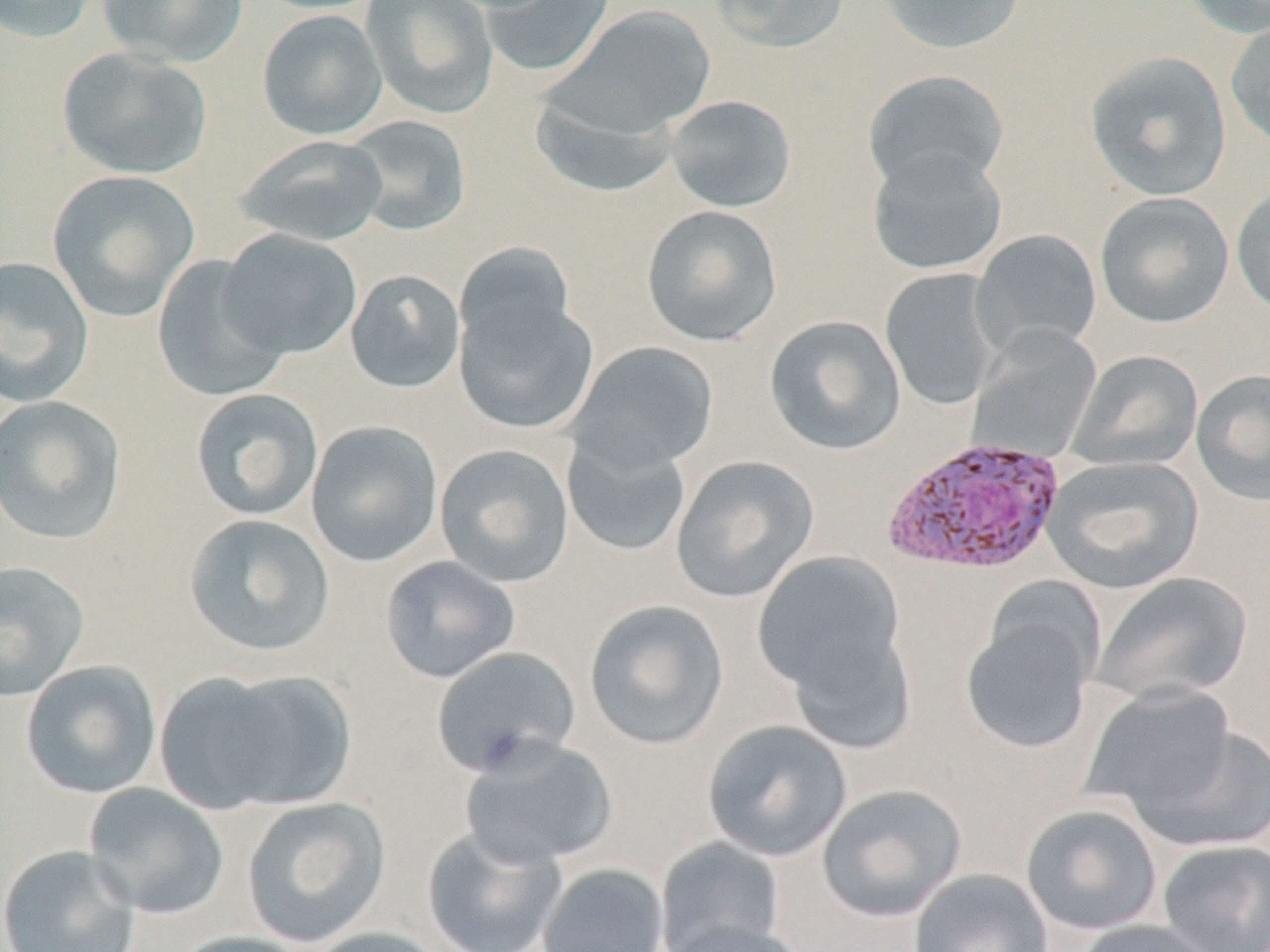
slide_level_diagnosis: Plasmodium vivax
magnification: 1000x
stain: May-Grünwald-Giemsa
preparation: thin blood smear
modality: optical microscopy
image_size: 1270×952 pixels
field_of_view: one of a larger specimen
plasmodium_vivax_infected_red_blood_cell_locations: 'approximate bounding boxes as named x1/y1/x2/y2 corners in pixels: (x1=881, y1=436, x2=1066, y2=577)'
uninfected_red_blood_cell_locations: 'approximate bounding boxes as named x1/y1/x2/y2 corners in pixels: (x1=0, y1=0, x2=101, y2=44), (x1=97, y1=0, x2=249, y2=68), (x1=252, y1=0, x2=389, y2=15), (x1=361, y1=0, x2=499, y2=120), (x1=478, y1=0, x2=616, y2=78), (x1=708, y1=0, x2=850, y2=54), (x1=877, y1=0, x2=1026, y2=55), (x1=1179, y1=0, x2=1270, y2=38), (x1=549, y1=5, x2=717, y2=139), (x1=256, y1=9, x2=388, y2=141), (x1=1226, y1=16, x2=1270, y2=151), (x1=56, y1=47, x2=212, y2=180), (x1=1084, y1=51, x2=1232, y2=202), (x1=862, y1=70, x2=1010, y2=196), (x1=530, y1=89, x2=679, y2=199), (x1=665, y1=95, x2=797, y2=213), (x1=341, y1=115, x2=472, y2=237), (x1=234, y1=134, x2=390, y2=247), (x1=867, y1=148, x2=1007, y2=276), (x1=47, y1=170, x2=200, y2=321), (x1=1231, y1=184, x2=1270, y2=317), (x1=1094, y1=192, x2=1235, y2=329), (x1=640, y1=204, x2=783, y2=347), (x1=218, y1=229, x2=362, y2=360), (x1=970, y1=229, x2=1103, y2=358), (x1=454, y1=243, x2=580, y2=359), (x1=151, y1=254, x2=291, y2=402), (x1=0, y1=256, x2=95, y2=408), (x1=880, y1=268, x2=1003, y2=410), (x1=344, y1=269, x2=466, y2=394), (x1=453, y1=286, x2=599, y2=436), (x1=764, y1=315, x2=906, y2=456), (x1=967, y1=325, x2=1103, y2=463), (x1=567, y1=341, x2=719, y2=474), (x1=1067, y1=350, x2=1203, y2=473), (x1=1191, y1=369, x2=1270, y2=505), (x1=190, y1=389, x2=324, y2=522), (x1=0, y1=395, x2=128, y2=545), (x1=305, y1=420, x2=444, y2=568), (x1=562, y1=432, x2=692, y2=558), (x1=434, y1=444, x2=576, y2=588), (x1=670, y1=454, x2=819, y2=603), (x1=1043, y1=455, x2=1204, y2=594), (x1=183, y1=514, x2=336, y2=657), (x1=753, y1=550, x2=909, y2=711), (x1=380, y1=556, x2=520, y2=683), (x1=0, y1=560, x2=90, y2=702), (x1=1091, y1=571, x2=1253, y2=706), (x1=960, y1=597, x2=1102, y2=756), (x1=583, y1=599, x2=730, y2=750), (x1=431, y1=645, x2=582, y2=778), (x1=20, y1=660, x2=162, y2=800), (x1=156, y1=668, x2=354, y2=815), (x1=1081, y1=683, x2=1240, y2=822), (x1=702, y1=719, x2=852, y2=862), (x1=1130, y1=722, x2=1270, y2=853), (x1=459, y1=737, x2=619, y2=870), (x1=82, y1=783, x2=230, y2=919), (x1=816, y1=783, x2=968, y2=923), (x1=240, y1=797, x2=391, y2=948), (x1=1021, y1=803, x2=1163, y2=935), (x1=421, y1=826, x2=567, y2=952), (x1=654, y1=837, x2=786, y2=951), (x1=1156, y1=840, x2=1270, y2=951), (x1=0, y1=845, x2=141, y2=952), (x1=537, y1=863, x2=670, y2=952), (x1=909, y1=867, x2=1054, y2=952), (x1=1072, y1=919, x2=1224, y2=952), (x1=661, y1=920, x2=810, y2=952), (x1=304, y1=926, x2=452, y2=952), (x1=171, y1=931, x2=318, y2=952)'